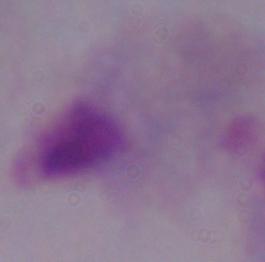 Captured at 1000x magnification. A trichomonad is seen. Micrograph.